Comment on the morphology of the erythrocytes.
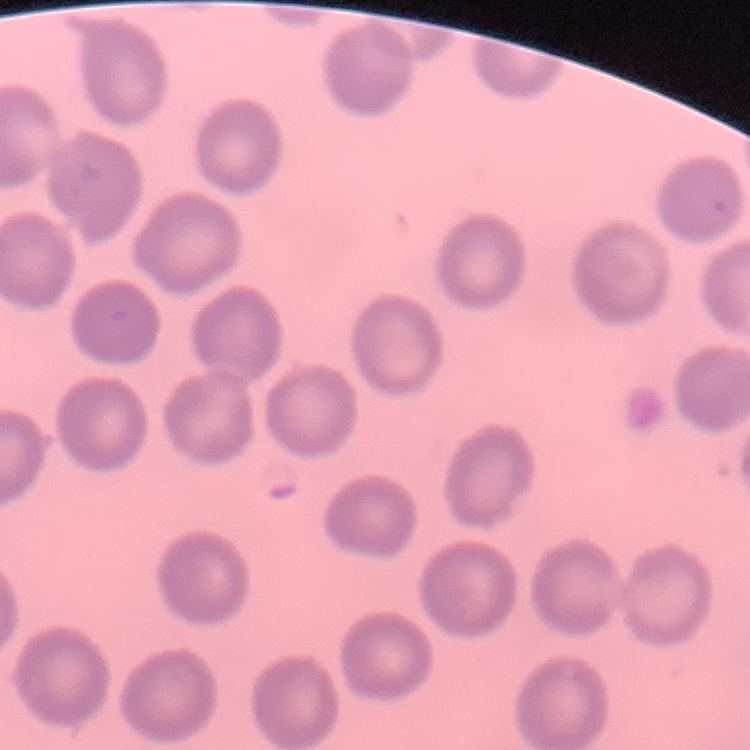
They show no rouleaux formation.

Summary:
  - Preparation: thin blood smear
  - Image type: square crop of a larger photomicrograph
  - Stain: Field's or Giemsa